Name the parasite shown.
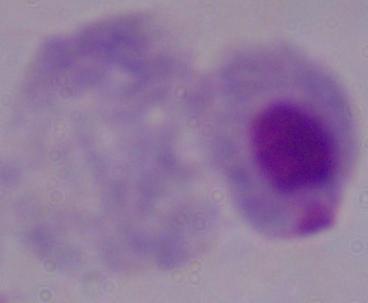

This is a trichomonad.

Captured at 1000x magnification. Photomicrograph.